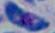

Summary:
  - Identification: Toxoplasma gondii
  - Modality: micrograph
  - Magnification: 1000x